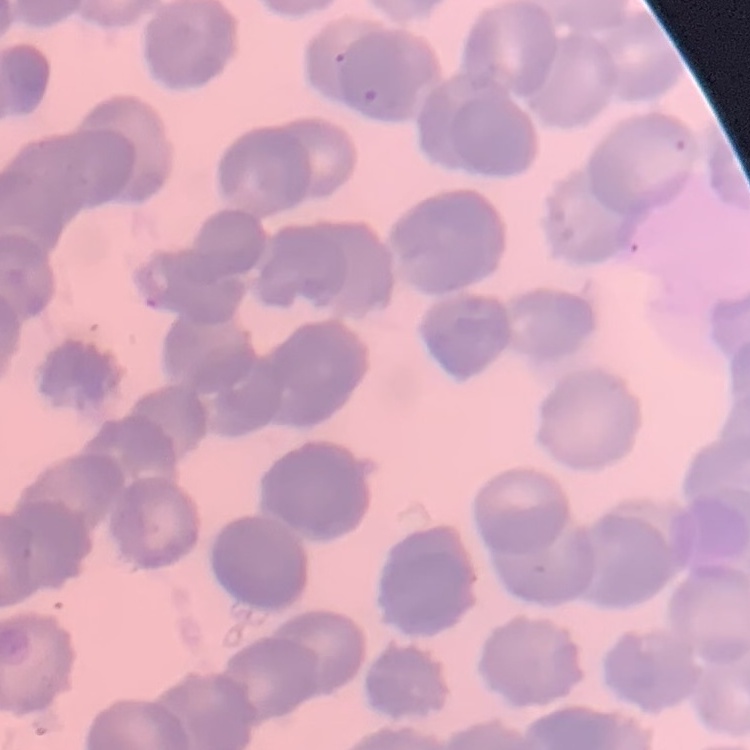 The erythrocytes show rouleaux formation. Thin blood film. One tile cut from a larger photomicrograph. Field's or Giemsa stain.